Locate and identify every blood parasite.
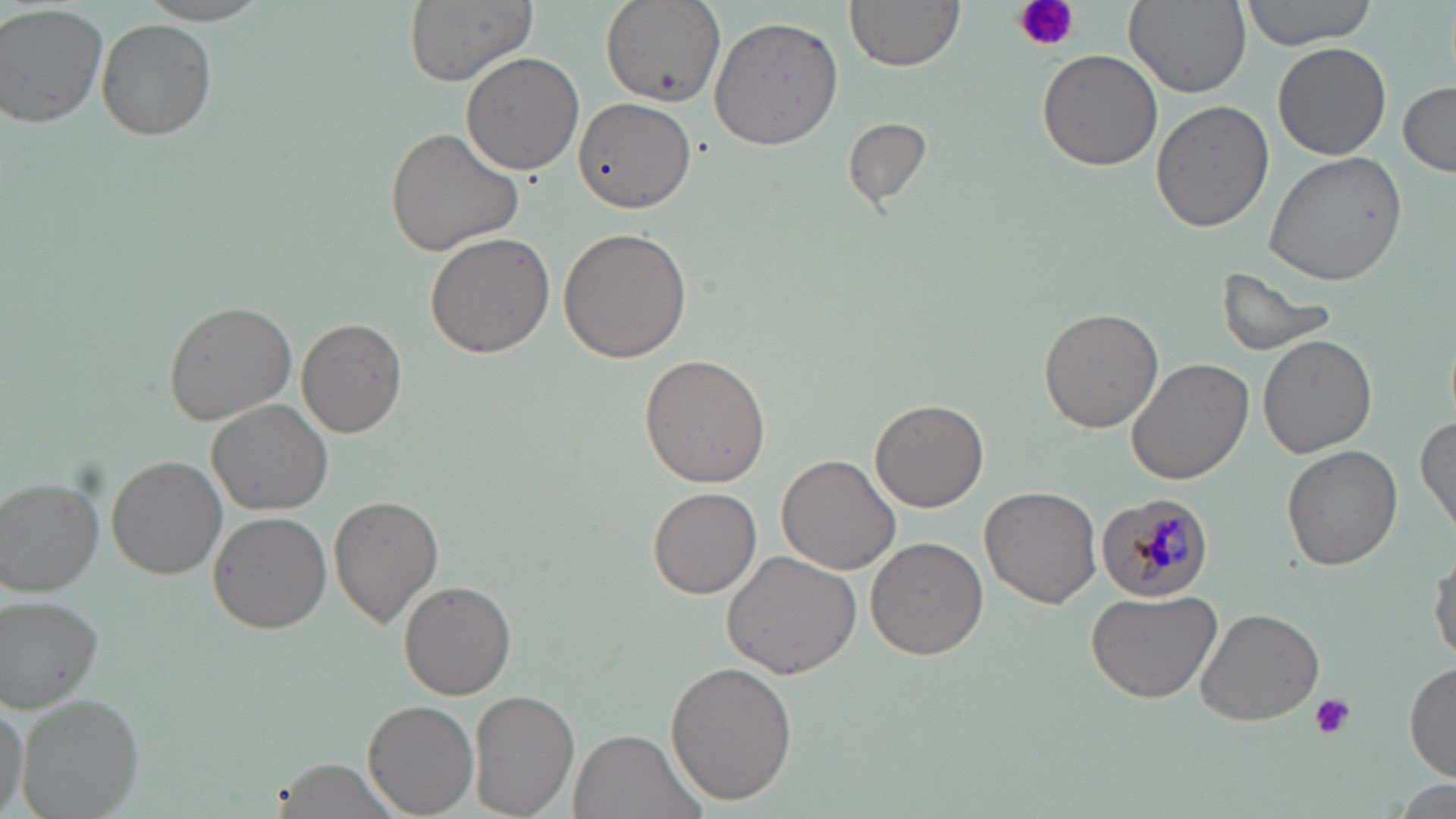
Approximate bounding boxes as (x1, y1, x2, y2) in pixels.
Plasmodium malariae-infected red blood cells: (1094, 494, 1217, 601).
No Plasmodium falciparum, Plasmodium ovale, Plasmodium vivax, Babesia divergens, or Trypanosoma brucei observed.

Uninfected red blood cell locations: (399, 0, 539, 86), (599, 0, 725, 107), (845, 0, 965, 71), (1125, 0, 1251, 96), (1237, 0, 1381, 51), (131, 1, 280, 25), (0, 5, 108, 129), (709, 16, 845, 149), (96, 19, 216, 140), (1273, 42, 1391, 160), (1037, 49, 1161, 172), (460, 52, 584, 174), (1398, 80, 1455, 176), (1150, 100, 1273, 233), (575, 101, 695, 213), (842, 116, 931, 207), (383, 126, 524, 257), (1266, 151, 1412, 285), (558, 227, 693, 363), (424, 231, 553, 359), (1216, 263, 1340, 357), (164, 299, 297, 426), (1039, 305, 1166, 432), (298, 319, 406, 438), (1258, 335, 1378, 459), (638, 353, 770, 488), (1127, 358, 1254, 485), (870, 397, 990, 512), (208, 398, 332, 515), (1415, 411, 1456, 535), (1281, 444, 1402, 571), (776, 453, 900, 575), (108, 457, 227, 578), (0, 477, 103, 595), (980, 485, 1104, 608), (649, 487, 761, 598), (330, 495, 444, 627), (208, 512, 331, 635), (865, 536, 987, 660), (1429, 549, 1456, 666), (724, 550, 863, 679), (401, 580, 516, 700), (1084, 588, 1222, 704), (1, 597, 107, 712), (1194, 606, 1325, 726), (667, 661, 798, 805), (1404, 662, 1456, 780), (471, 690, 580, 819), (0, 693, 29, 817), (16, 693, 144, 819), (363, 699, 479, 816), (569, 730, 705, 819), (273, 757, 405, 819). Platelet locations: (1014, 0, 1079, 55), (1309, 691, 1355, 739). Slide-level diagnosis: Plasmodium malariae. Thin blood film. Single field of view. Image is 1456×819 pixels. Optical microscopy. 1000x magnification. May-Grünwald-Giemsa stain.